Classify this cell by malaria status.
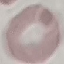

Uninfected.

{
  "preparation": "thin smear",
  "image_type": "automatically extracted cell patch, resized to 64 × 64 pixels",
  "stain": "Giemsa",
  "capture": "smartphone through the microscope eyepiece"
}